Give the position of every Plasmodium parasite.
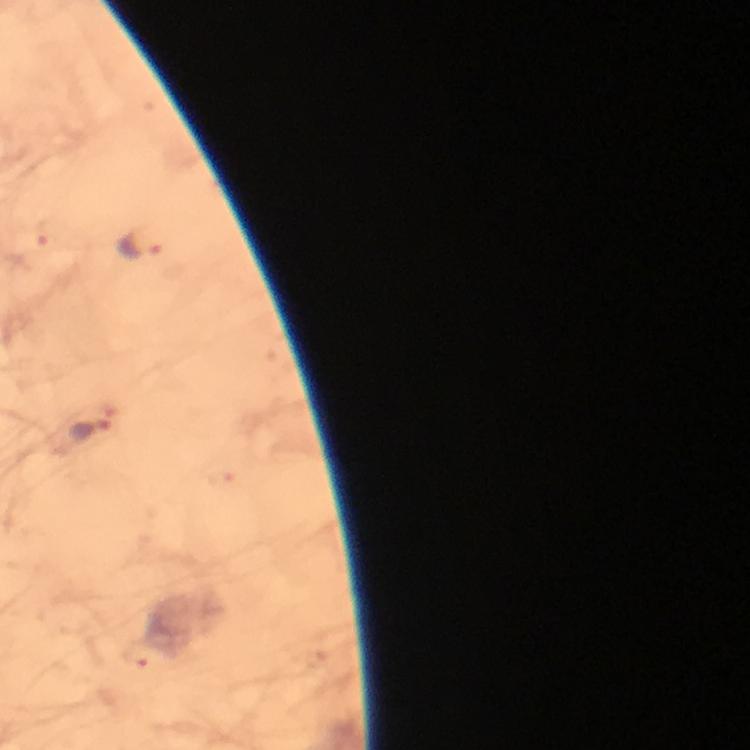
Approximate centers as [x, y] in pixels.
Plasmodium parasites: [138, 247], [90, 432].

Summary:
  - Preparation: thick smear
  - Stain: Giemsa
  - Magnification: 100x
  - Image size: 750×750 pixels
  - Immersion oil: used
  - Capture: smartphone mounted on the microscope
  - Context: from a diagnostic examination for malaria
  - Cropped from: one field of view